Classify this cell by malaria status.
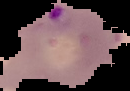
Parasitized.

{
  "image_size": "130×91 pixels",
  "preparation": "thin blood film",
  "image_type": "segmented cell region on a black background"
}